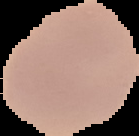
preparation = thin blood film
image type = segmented cell region with the area outside set to black
result = negative for malaria parasites
image size = 139×136 pixels